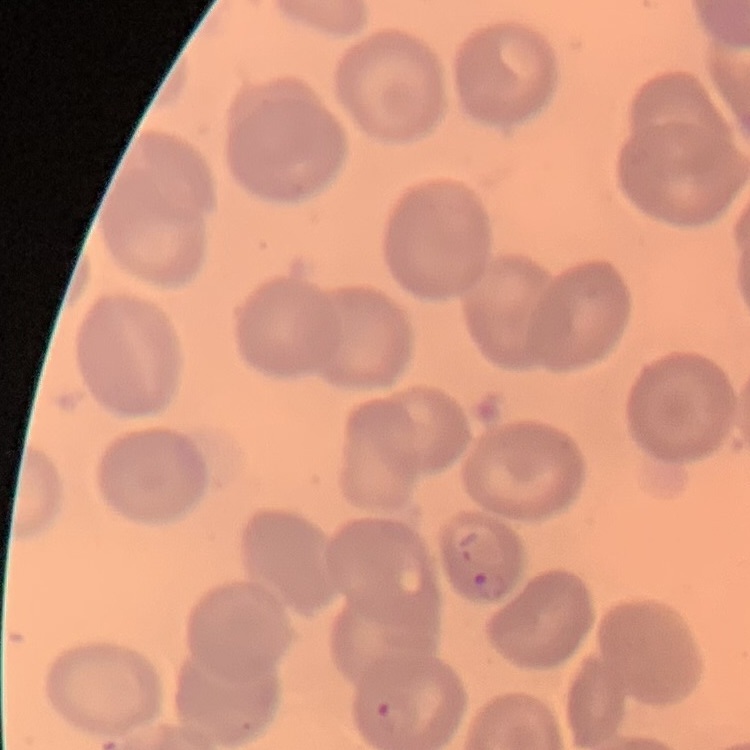

erythrocyte morphology = no rouleaux formation
preparation = thin peripheral smear
image type = one tile cut from a larger photomicrograph
stain = Field's or Giemsa